Assess the morphology of the erythrocytes.
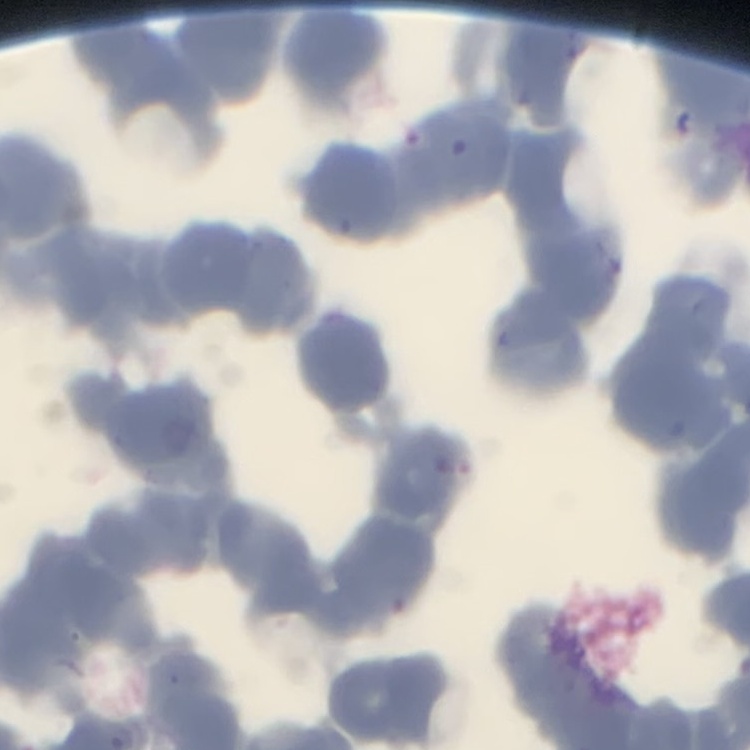

Rouleaux formation.

One tile cut from a larger photomicrograph. Thin blood smear. Stained with either Field's or Giemsa.